State which parasite is depicted.
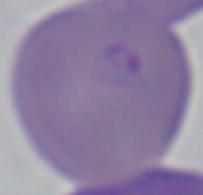
Babesia.

magnification = 1000x
modality = photomicrograph